Look for parasitized red blood cells.
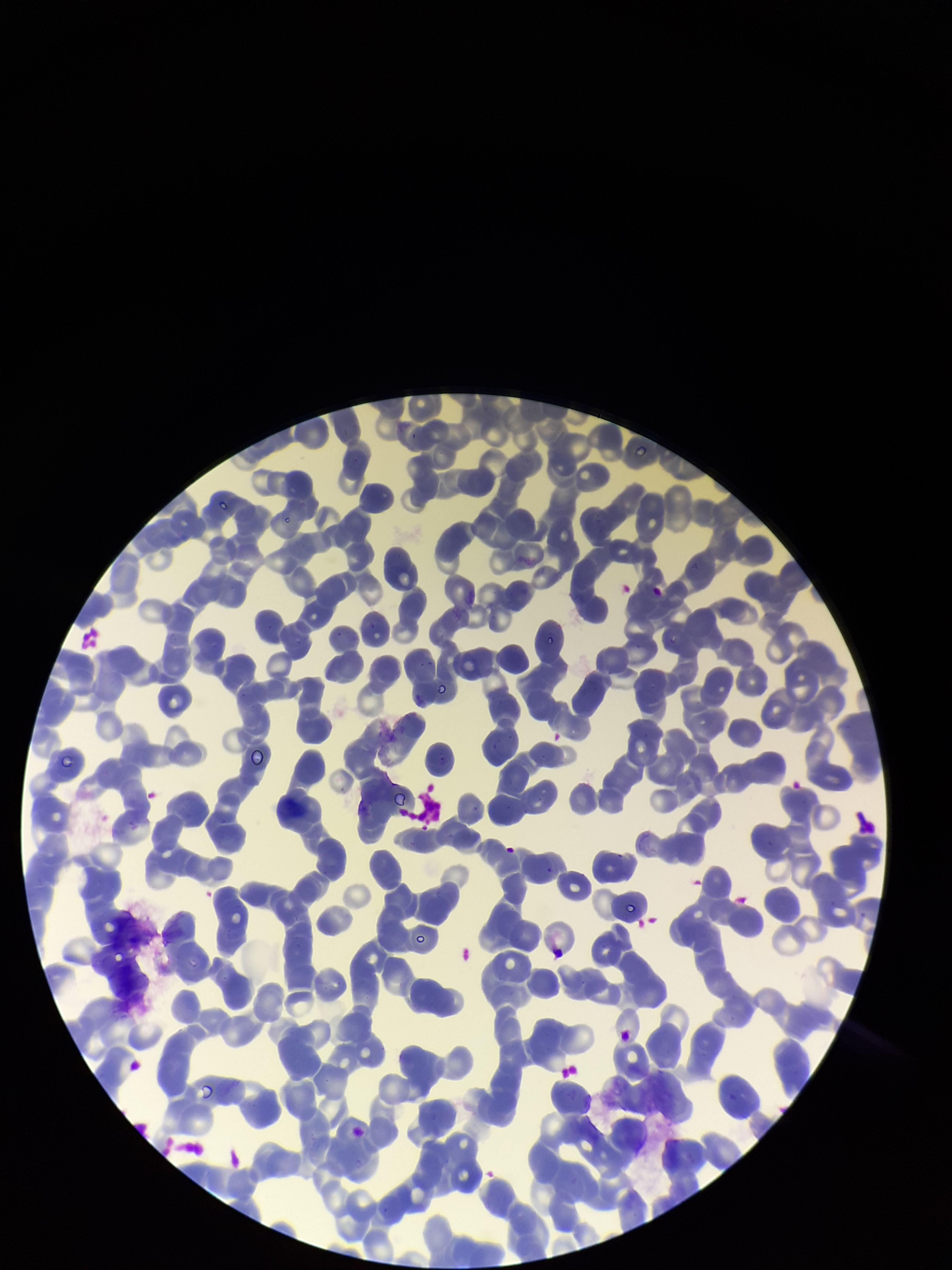

None identified.

Summary:
  - Capture: smartphone photograph through the microscope eyepiece
  - Patient malaria status: negative
  - Parasitized red blood cell count: 0
  - Field of view: one from this slide
  - Stain: Giemsa
  - Red blood cell count: 261
  - Image size: 952×1270 pixels
  - Preparation: thin smear